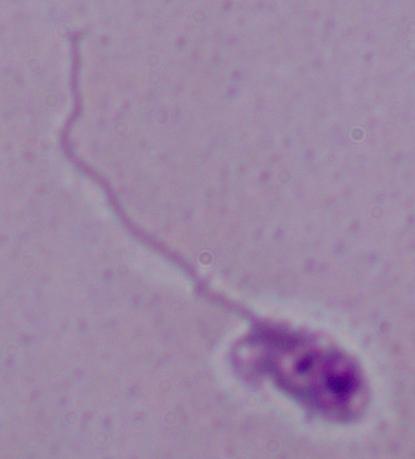
Summary:
  - Modality: photomicrograph
  - Magnification: 1000x
  - Identification: Leishmania